Comment on the morphology of the erythrocytes.
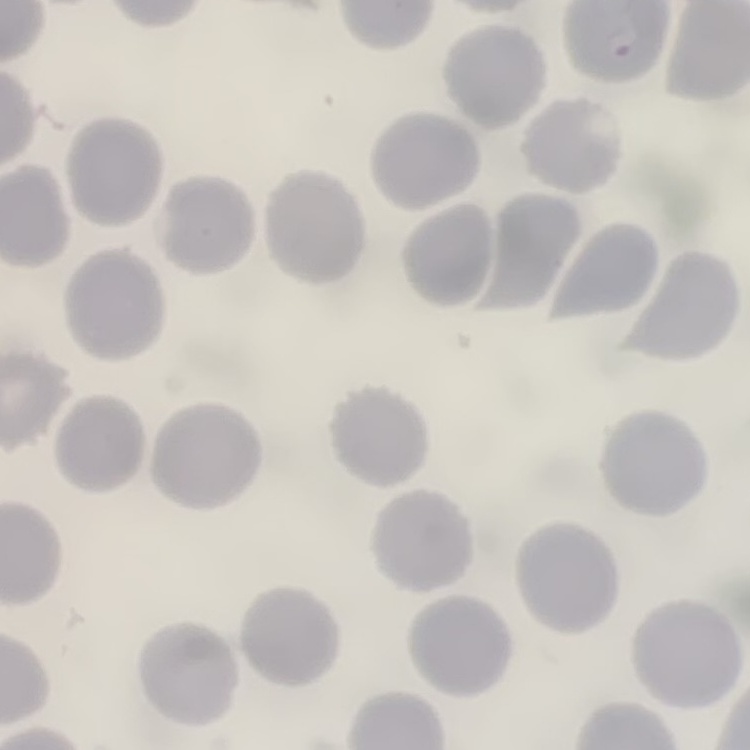

They show no rouleaux formation.

Summary:
  - Stain: Field's or Giemsa
  - Image type: one tile cut from a larger photomicrograph
  - Preparation: thin blood film